Give the extent of all uninfected red blood cells.
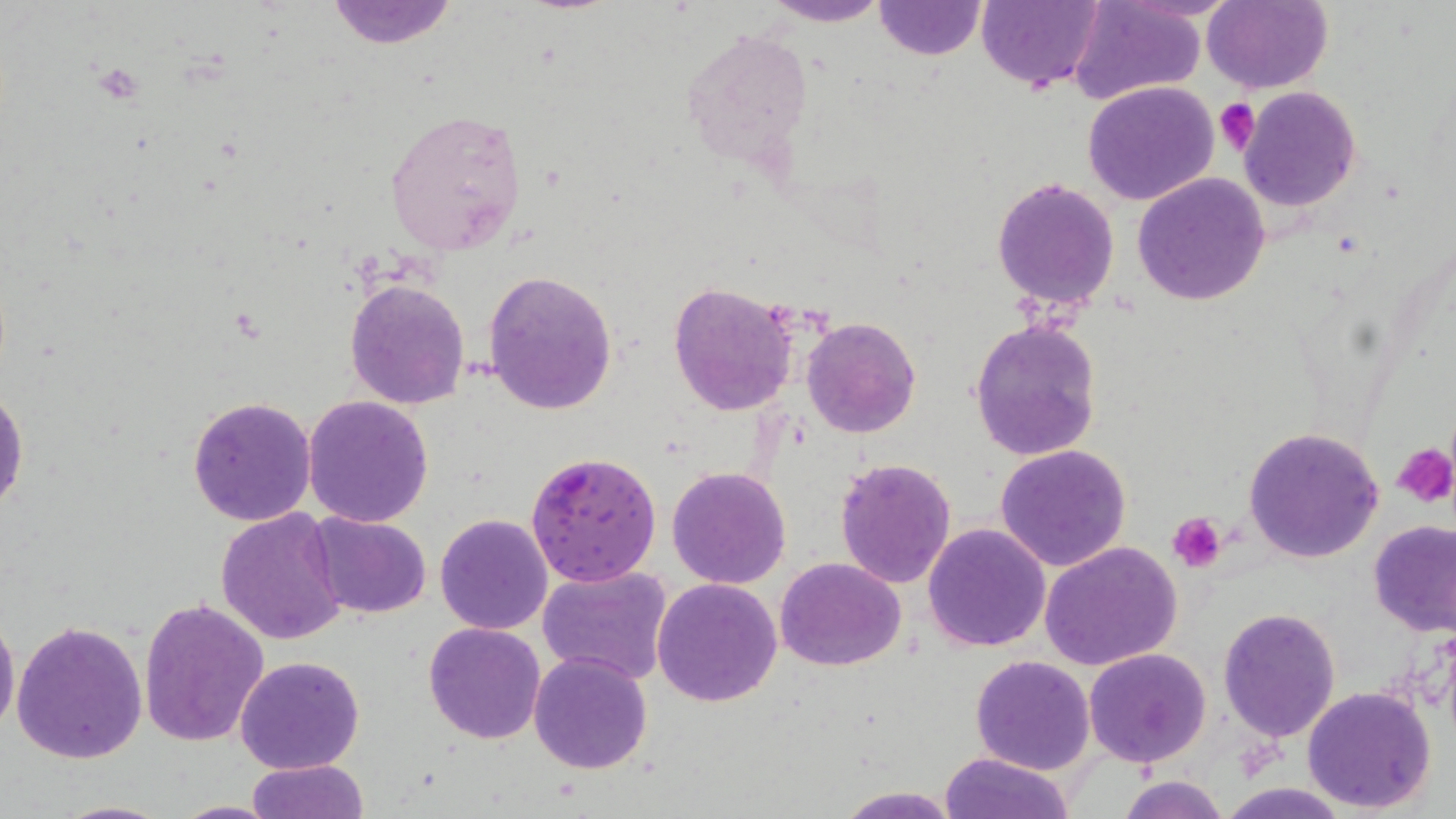

Approximate bounding boxes as (x1,y1)-(x2,y2) corner pairs in pixels.
Uninfected red blood cells: (325,0)-(459,49), (762,0)-(892,26), (875,0)-(983,59), (975,0)-(1103,92), (1202,0)-(1332,93), (1070,1)-(1205,106), (678,21)-(816,169), (1083,81)-(1220,206), (1239,89)-(1361,211), (384,107)-(527,254), (1133,173)-(1271,305), (991,176)-(1120,313), (484,270)-(619,416), (345,278)-(471,408), (669,281)-(796,416), (801,317)-(920,439), (968,318)-(1103,460), (0,386)-(28,516), (303,394)-(435,527), (187,395)-(317,526), (1244,426)-(1385,563), (994,444)-(1132,572), (834,458)-(958,589), (666,465)-(792,589), (215,508)-(348,647), (309,512)-(432,619), (434,513)-(554,635), (1369,522)-(1456,636), (922,523)-(1052,652), (1039,541)-(1183,671), (775,557)-(906,672), (538,563)-(673,685), (652,578)-(783,706), (138,598)-(270,747), (1218,607)-(1342,742), (0,615)-(20,735), (11,618)-(149,764), (423,622)-(546,744), (1084,647)-(1213,767), (528,652)-(653,774), (235,655)-(365,773), (970,655)-(1095,774), (1303,685)-(1438,814), (939,752)-(1078,819), (246,758)-(367,819), (1118,775)-(1230,819), (1218,782)-(1349,818), (833,785)-(962,818), (52,800)-(178,818), (166,801)-(289,819).

Platelet locations: (1215,97)-(1260,156), (1392,443)-(1456,508), (1169,514)-(1226,572). Plasmodium falciparum-infected red blood cell locations: (526,451)-(662,584). Slide-level diagnosis: Plasmodium falciparum. Light microscopy. One field of a larger specimen. Image is 1456×819 pixels. Thin blood smear. May-Grünwald-Giemsa-stained preparation. 1000x magnification.